Identify the cell.
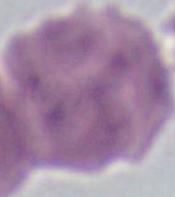

An erythrocyte.

magnification = 1000x
modality = photomicrograph